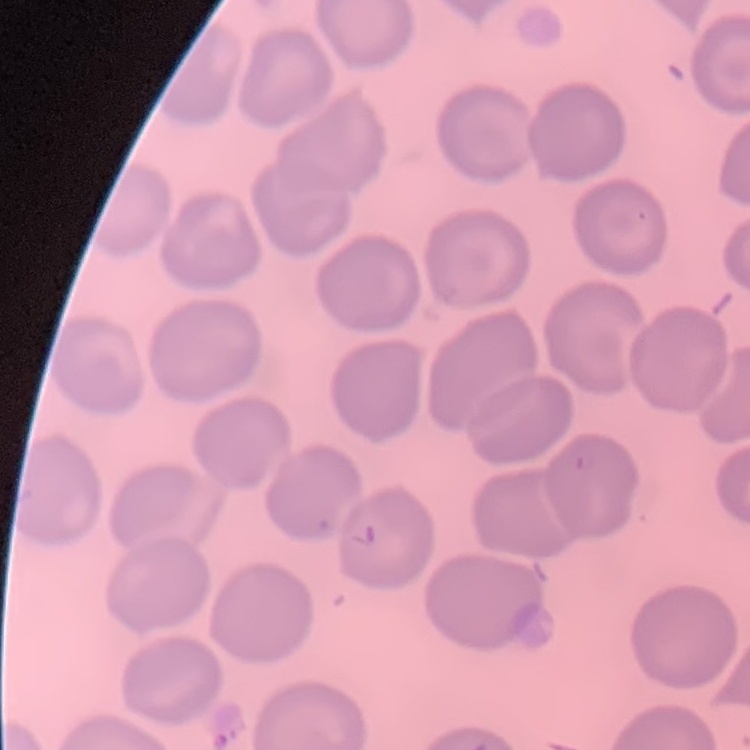

erythrocyte_morphology: no rouleaux formation
image_type: square crop of a larger photomicrograph
stain: Field's or Giemsa
preparation: thin blood film